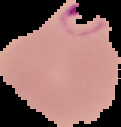

Summary:
  - Image size: 121×127 pixels
  - Preparation: thin blood smear
  - Result: Plasmodium parasites identified
  - Image type: segmented cell region on a black background